Describe the morphology of the erythrocytes.
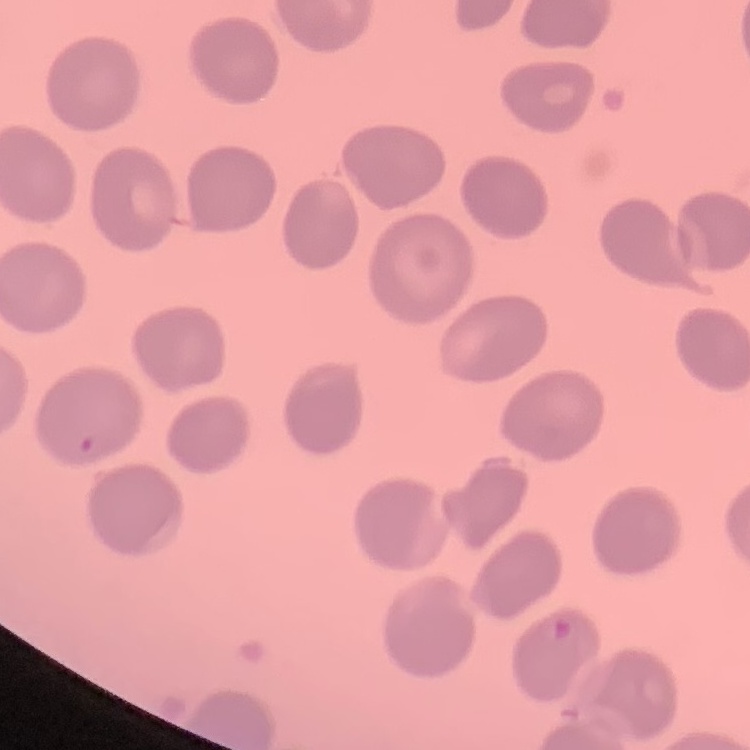

No rouleaux formation.

Thin peripheral smear. Square crop of a larger photomicrograph. Field's or Giemsa stain.